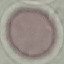
{
  "result": "no malaria parasites detected",
  "image_type": "automatically extracted cell patch, resized to 64 × 64 pixels",
  "preparation": "thin blood smear",
  "capture": "smartphone through the microscope eyepiece",
  "stain": "Giemsa"
}